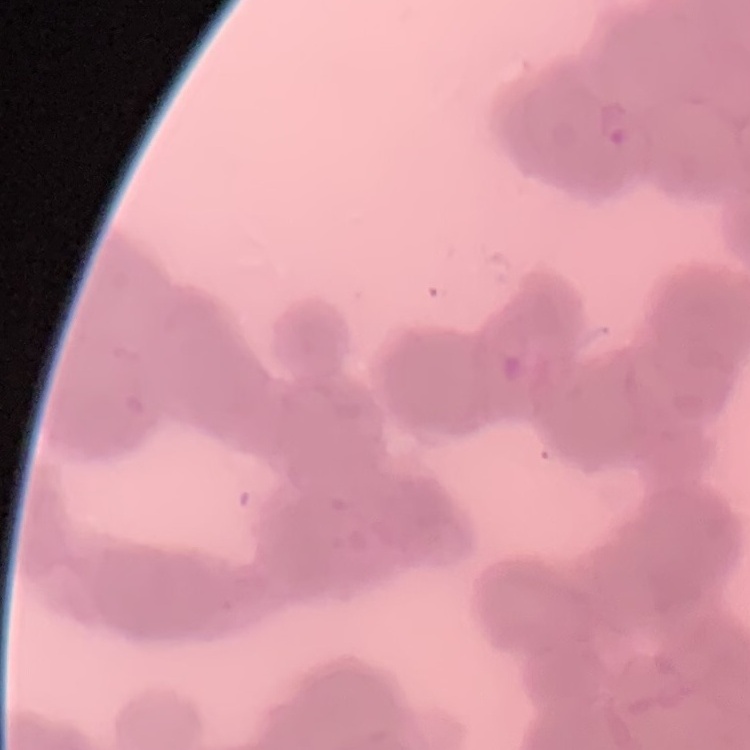
The red blood cells exhibit rouleaux formation. Square crop of a larger photomicrograph. Thin peripheral smear. Field's or Giemsa stain.